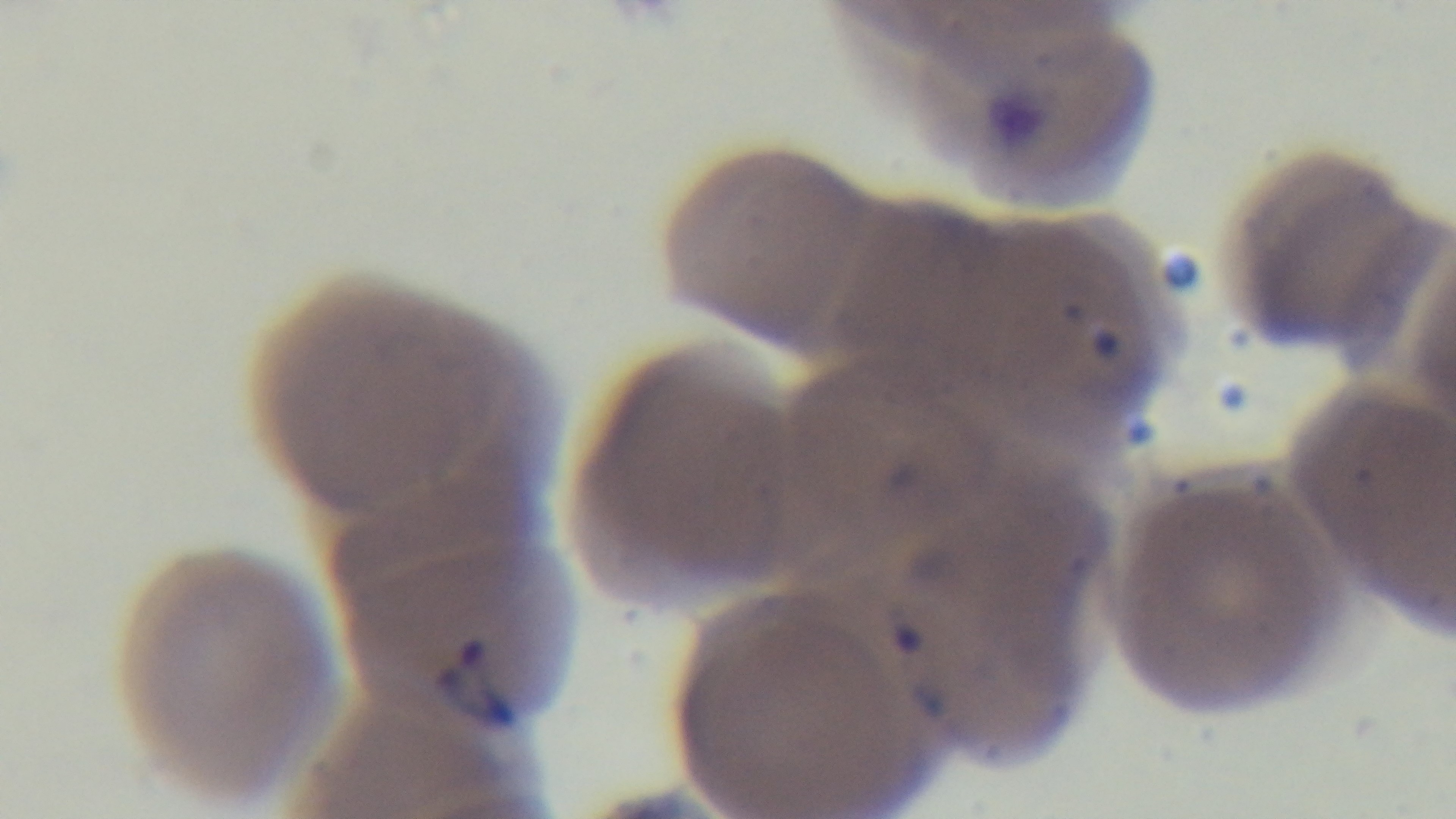 Preparation: thin smear. Malaria status: positive. Mounted 4K digital camera. Photomicrograph. Oil-immersion objective, 100x. Single field of view. Giemsa-stained.